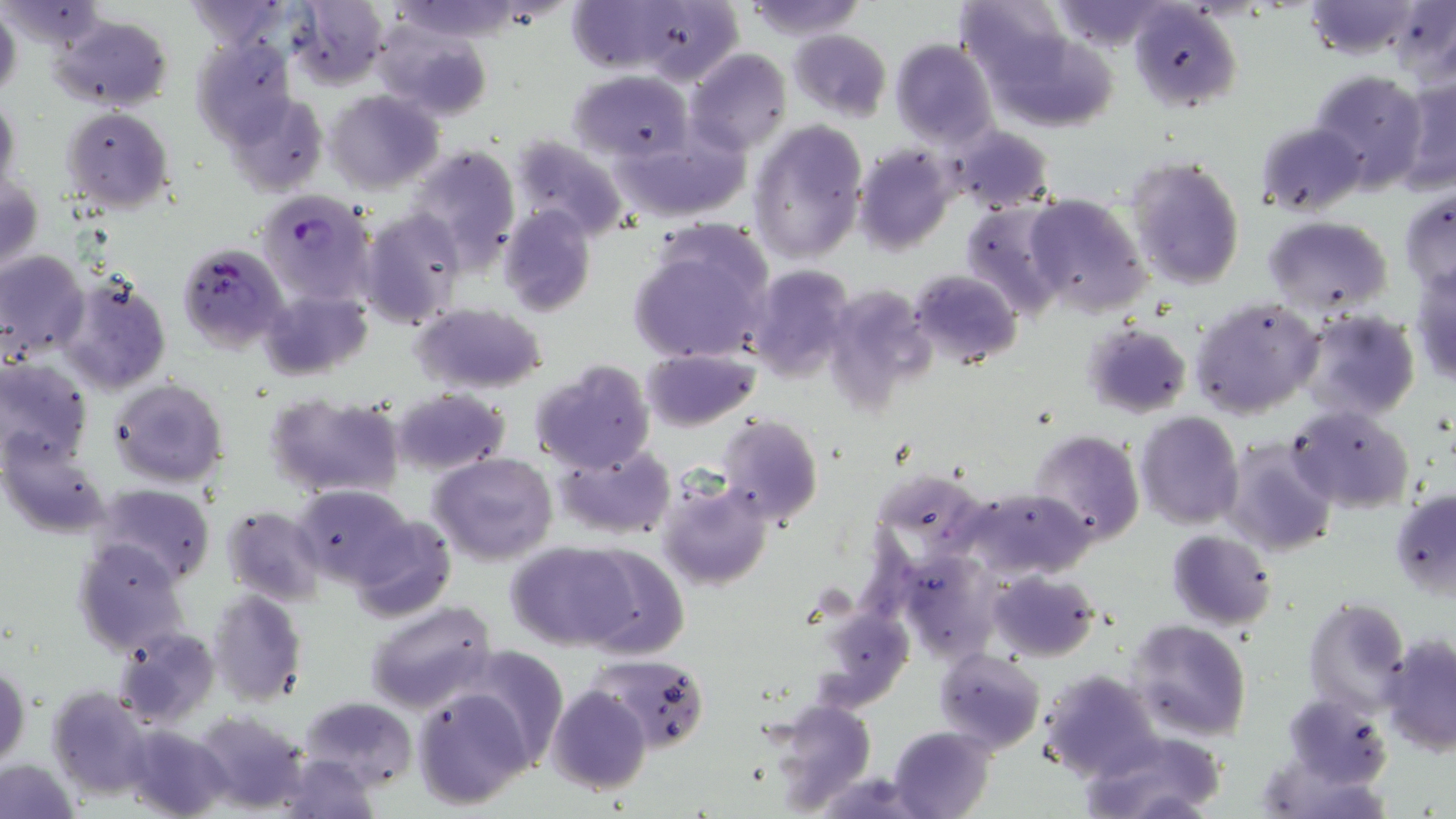

{
  "slide_level_diagnosis": "Plasmodium falciparum",
  "preparation": "thin blood smear",
  "stain": "May-Grünwald-Giemsa",
  "image_size": "1456×819 pixels",
  "modality": "optical microscopy",
  "uninfected_red_blood_cell_locations": "approximate bounding boxes as (x1,y1)-(x2,y2) corner pairs in pixels: (742,0)-(866,39), (957,0)-(1073,96), (1300,0)-(1430,59), (1390,0)-(1456,87), (176,1)-(293,46), (289,1)-(388,87), (1047,1)-(1174,50), (2,2)-(108,53), (569,2)-(740,83), (1128,2)-(1241,112), (0,6)-(21,102), (52,13)-(174,113), (372,24)-(491,122), (790,29)-(891,121), (194,39)-(300,147), (889,39)-(997,146), (686,49)-(790,156), (569,70)-(692,162), (1309,70)-(1427,191), (1397,72)-(1456,194), (327,89)-(444,194), (227,93)-(329,196), (1,95)-(20,195), (61,107)-(175,212), (1255,120)-(1366,217), (748,121)-(868,264), (612,124)-(747,223), (944,124)-(1053,214), (510,137)-(626,241), (405,144)-(521,272), (851,146)-(954,253), (1126,156)-(1247,291), (1,176)-(43,272), (1398,184)-(1455,297), (1024,194)-(1150,317), (957,201)-(1066,316), (499,204)-(596,317), (357,208)-(464,330), (1263,215)-(1393,313), (628,235)-(773,366), (0,250)-(89,360), (745,263)-(855,384), (1409,267)-(1456,386), (909,269)-(1021,368), (55,273)-(171,396), (821,279)-(941,410), (260,290)-(372,381), (1190,298)-(1323,419), (413,304)-(546,394), (1297,309)-(1421,421), (1082,323)-(1192,419), (641,349)-(759,430), (0,357)-(93,469), (530,359)-(655,475), (109,378)-(228,488), (389,388)-(510,476), (265,392)-(406,499), (1286,404)-(1414,513), (1135,411)-(1244,529), (716,414)-(823,527), (1026,429)-(1144,546), (2,438)-(114,538), (1224,438)-(1335,557), (552,442)-(676,540), (431,453)-(559,567), (655,477)-(772,590), (95,483)-(216,587), (954,485)-(1096,581), (291,486)-(421,592), (1391,488)-(1456,597), (222,506)-(324,603), (346,515)-(455,622), (1166,529)-(1277,630), (74,537)-(189,657), (504,542)-(634,651), (571,546)-(689,660), (894,547)-(1002,663), (986,570)-(1099,660), (208,586)-(307,707), (1302,596)-(1410,714), (812,598)-(910,707), (363,600)-(495,714), (1128,619)-(1252,741), (113,629)-(221,727), (1380,635)-(1456,755), (934,647)-(1045,753), (590,654)-(710,751), (1,665)-(28,768), (1038,667)-(1163,782), (547,685)-(651,795), (411,686)-(533,809), (47,687)-(154,799), (1283,693)-(1393,788), (299,696)-(416,789), (765,704)-(877,809), (189,710)-(310,810), (122,726)-(233,818), (890,726)-(995,819), (1081,731)-(1227,817), (276,751)-(380,818), (0,757)-(80,817)",
  "plasmodium_falciparum_infected_red_blood_cell_locations": "approximate bounding boxes as (x1,y1)-(x2,y2) corner pairs in pixels: (253,190)-(376,313), (177,242)-(289,351)",
  "field_of_view": "single",
  "magnification": "1000x"
}